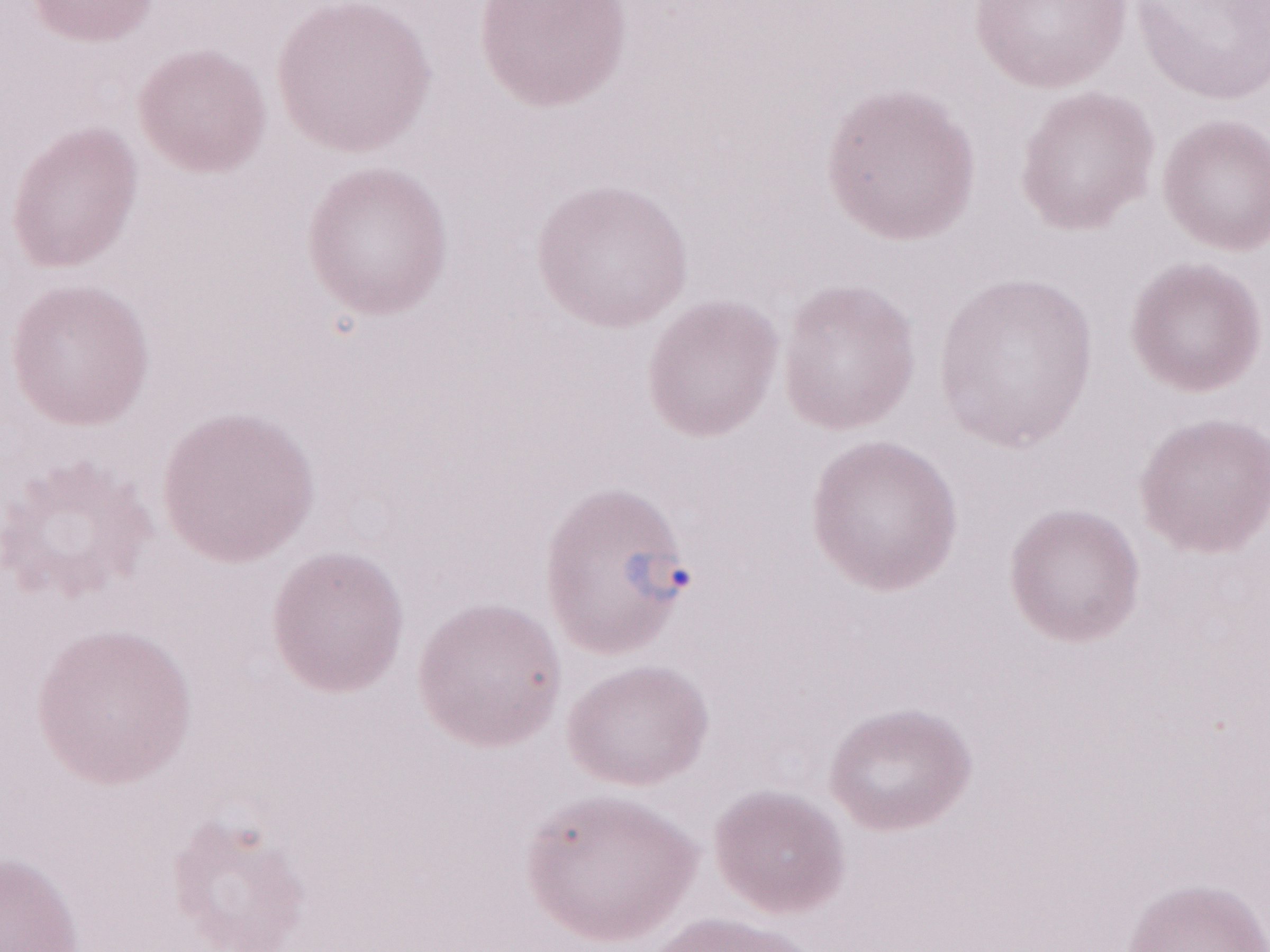
May-Grünwald-Giemsa (MGG) stain. Image is 1270×952 pixels. Thin peripheral-blood smear. Olympus BX43 microscope, Olympus DP73 camera. Single field of view. Patient diagnosis: malaria infection. 1,000x magnification.